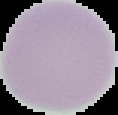

{
  "image_type": "segmented cell region with the area outside set to black",
  "image_size": "118×115 pixels",
  "result": "no malaria parasites detected",
  "preparation": "thin blood smear"
}